Report the malaria status.
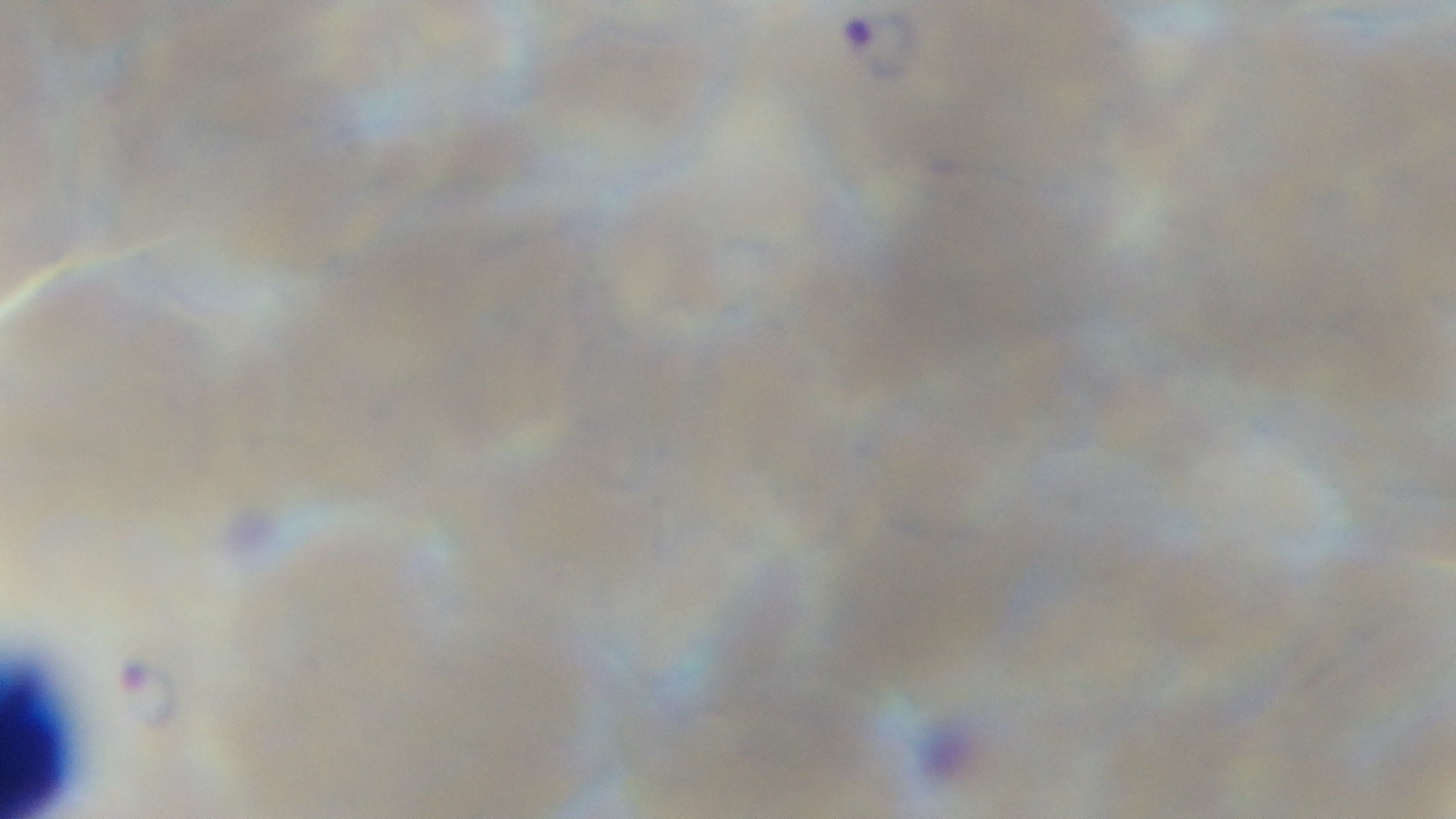

Infected.

Summary:
  - Objective: 100x oil immersion
  - Preparation: thin blood film
  - Capture: mounted 4K digital camera
  - Modality: light microscopy
  - Stain: Giemsa
  - Field of view: one from the slide